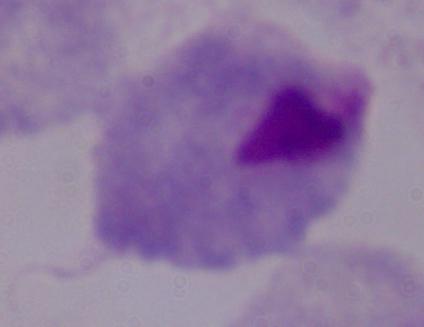
Photomicrograph. A trichomonad is shown. Captured at 1000x magnification.